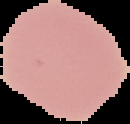 The area outside the segmented cell region is set to black. Image is 130×124 pixels. Result: negative for malaria parasites. From a thin blood film.